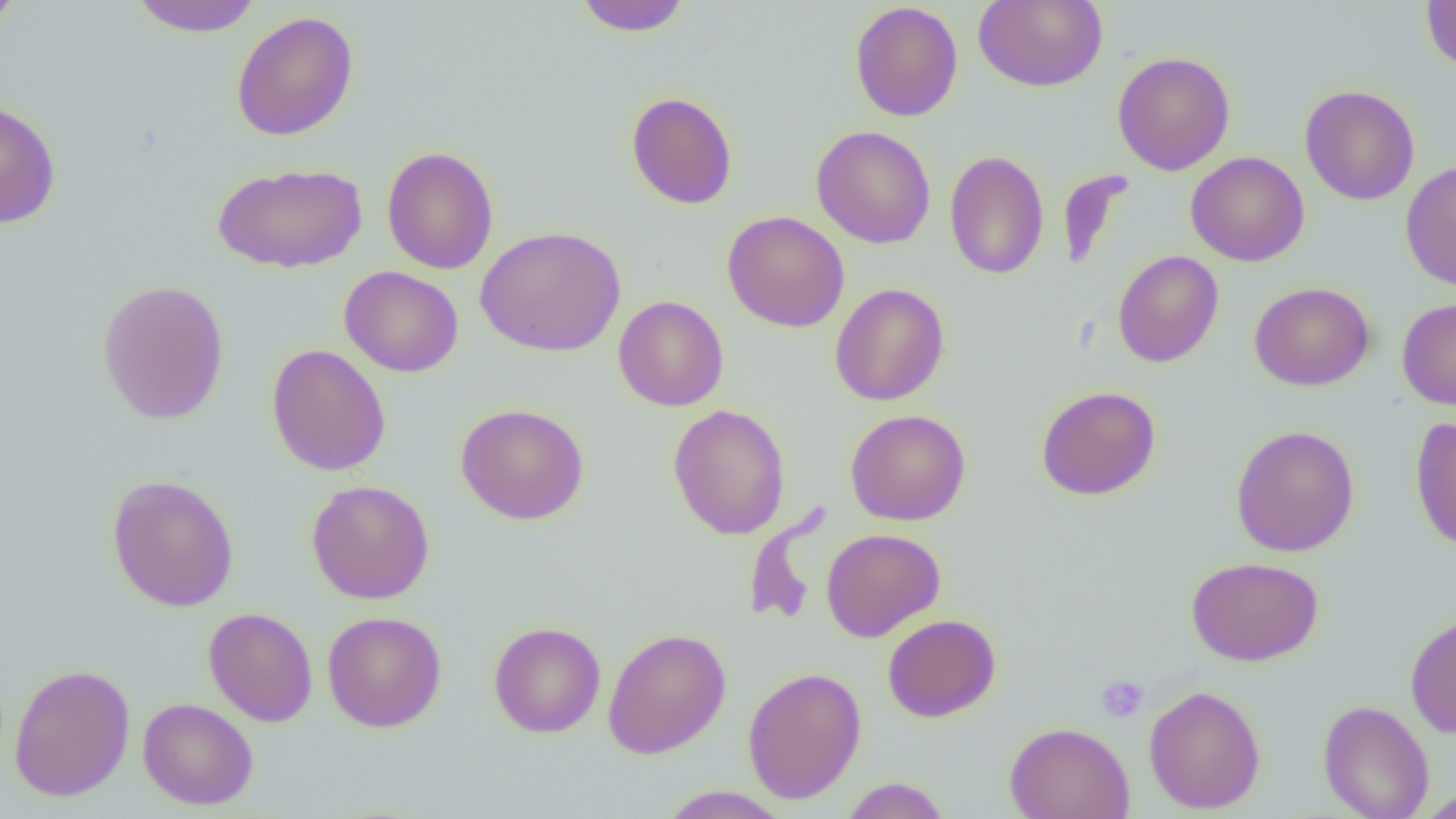
{
  "slide_level_diagnosis": "no evidence of blood parasites",
  "field_of_view": "one of a larger specimen",
  "uninfected_red_blood_cell_locations": "approximate bounding boxes as named x1/y1/x2/y2 corners in pixels: (x1=0, y1=0, x2=24, y2=35), (x1=128, y1=0, x2=263, y2=37), (x1=573, y1=0, x2=693, y2=37), (x1=973, y1=0, x2=1107, y2=92), (x1=1421, y1=1, x2=1455, y2=75), (x1=849, y1=2, x2=963, y2=122), (x1=231, y1=11, x2=359, y2=141), (x1=1112, y1=51, x2=1235, y2=175), (x1=1300, y1=85, x2=1420, y2=205), (x1=626, y1=91, x2=738, y2=210), (x1=0, y1=98, x2=62, y2=229), (x1=811, y1=125, x2=936, y2=249), (x1=381, y1=146, x2=499, y2=274), (x1=944, y1=150, x2=1049, y2=280), (x1=1186, y1=151, x2=1309, y2=267), (x1=1399, y1=160, x2=1456, y2=291), (x1=212, y1=162, x2=367, y2=273), (x1=1059, y1=170, x2=1133, y2=273), (x1=721, y1=211, x2=850, y2=333), (x1=476, y1=225, x2=626, y2=357), (x1=1113, y1=249, x2=1224, y2=368), (x1=339, y1=266, x2=464, y2=378), (x1=96, y1=279, x2=230, y2=425), (x1=831, y1=282, x2=949, y2=406), (x1=1249, y1=282, x2=1375, y2=391), (x1=613, y1=295, x2=729, y2=412), (x1=1396, y1=297, x2=1456, y2=409), (x1=266, y1=344, x2=391, y2=476), (x1=1036, y1=386, x2=1161, y2=501), (x1=455, y1=403, x2=589, y2=525), (x1=667, y1=404, x2=791, y2=540), (x1=845, y1=409, x2=972, y2=526), (x1=1410, y1=416, x2=1456, y2=551), (x1=1230, y1=425, x2=1360, y2=557), (x1=106, y1=474, x2=239, y2=612), (x1=307, y1=480, x2=435, y2=604), (x1=743, y1=504, x2=830, y2=628), (x1=821, y1=528, x2=946, y2=642), (x1=1186, y1=556, x2=1323, y2=666), (x1=203, y1=607, x2=318, y2=727), (x1=323, y1=611, x2=447, y2=733), (x1=1405, y1=611, x2=1456, y2=738), (x1=883, y1=614, x2=1001, y2=722), (x1=489, y1=621, x2=606, y2=738), (x1=602, y1=627, x2=731, y2=759), (x1=9, y1=663, x2=135, y2=801), (x1=742, y1=666, x2=866, y2=804), (x1=1144, y1=684, x2=1266, y2=814), (x1=138, y1=698, x2=258, y2=810), (x1=1318, y1=700, x2=1434, y2=819), (x1=1005, y1=722, x2=1134, y2=819), (x1=841, y1=777, x2=950, y2=819), (x1=657, y1=786, x2=792, y2=818), (x1=1417, y1=787, x2=1456, y2=819)",
  "image_size": "1456×819 pixels",
  "magnification": "1000x",
  "preparation": "thin blood film",
  "platelet_locations": "approximate bounding boxes as named x1/y1/x2/y2 corners in pixels: (x1=1095, y1=675, x2=1148, y2=724)",
  "modality": "optical microscopy"
}